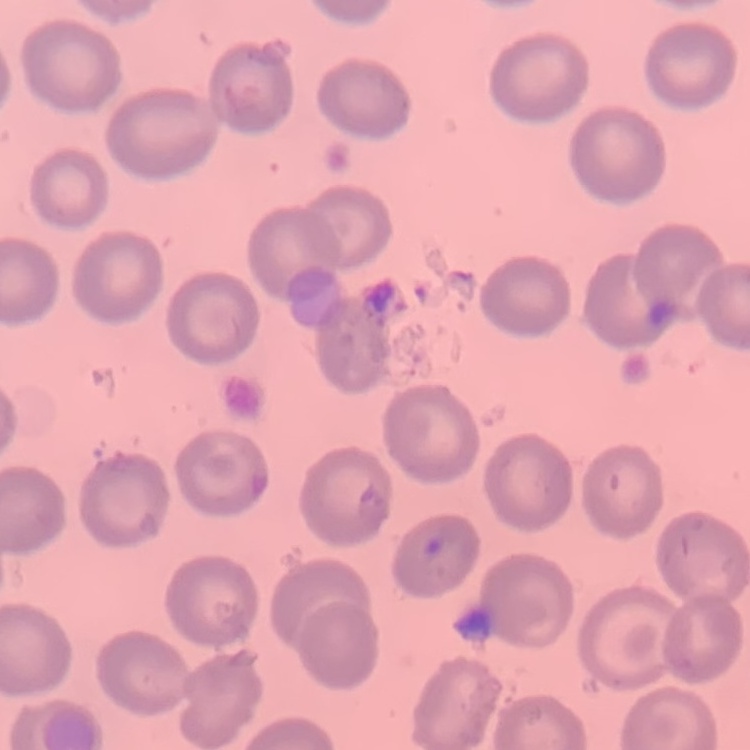
red blood cell morphology = no rouleaux formation
image type = one tile cut from a larger photomicrograph
preparation = thin blood smear
stain = Field's or Giemsa